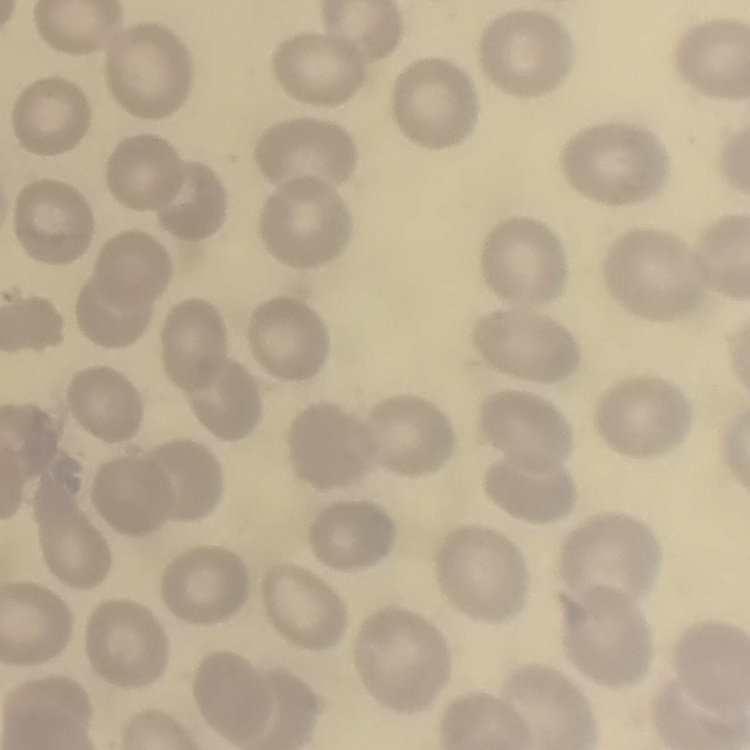

The red blood cells show no rouleaux formation. Thin blood smear. One tile cut from a larger photomicrograph. Stained with either Field's or Giemsa.